Locate every Plasmodium parasite and every leukocyte.
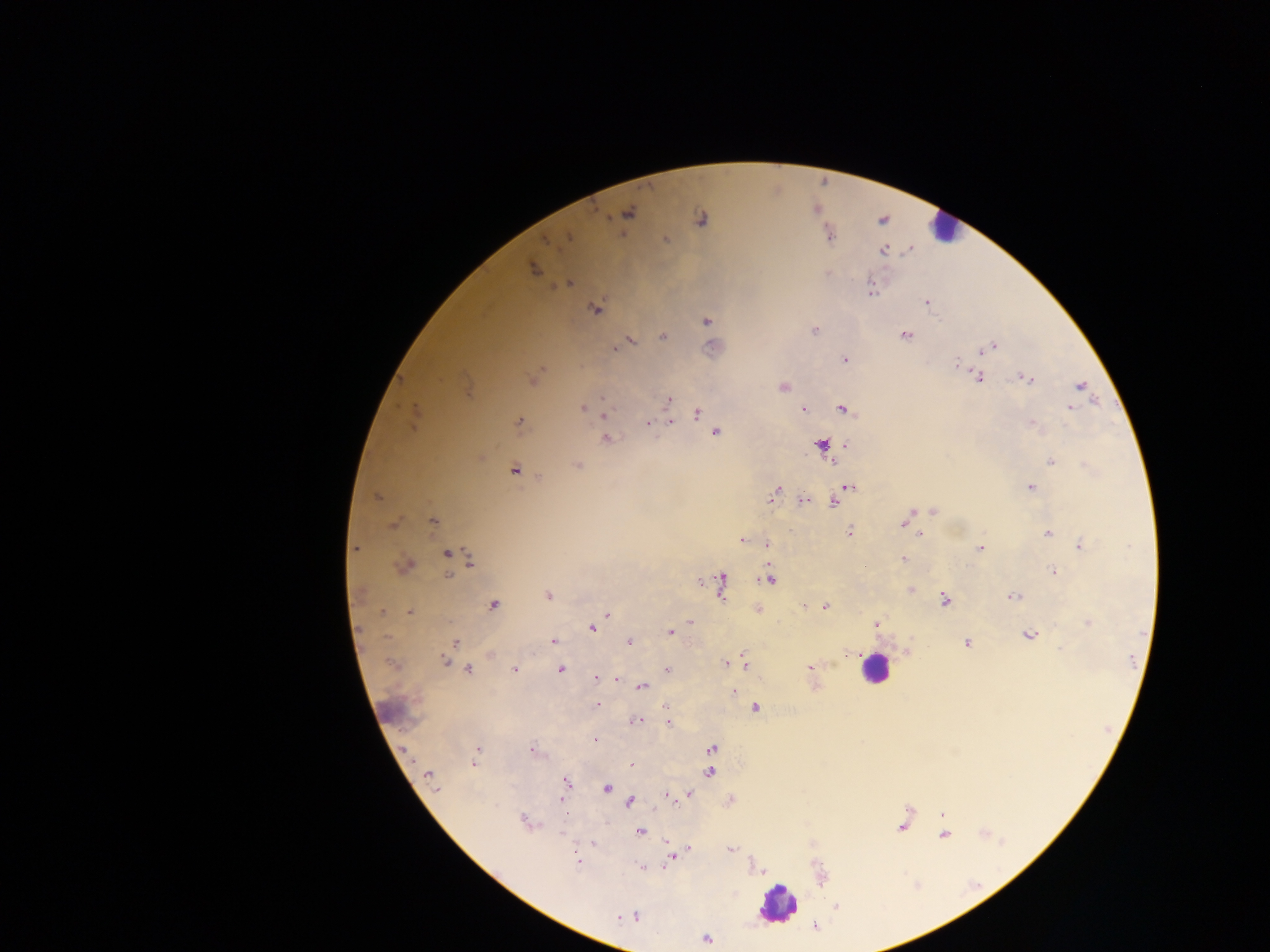

Approximate centers as (x, y) in pixels.
Plasmodium parasites: (627, 213), (701, 219), (829, 236), (568, 238), (665, 239), (884, 251), (533, 270), (569, 283), (871, 292), (927, 302), (595, 309), (707, 321), (815, 331), (905, 335), (663, 336), (631, 340), (714, 347), (993, 347), (614, 349), (984, 350), (844, 360), (956, 363), (978, 377), (1027, 379), (534, 380), (1080, 385), (783, 387), (668, 400), (603, 406), (1070, 407), (582, 408), (843, 409), (804, 411), (414, 414), (696, 414), (604, 415), (519, 421), (670, 421), (648, 423), (1032, 423), (715, 433), (606, 437), (821, 445), (847, 445), (1051, 462), (577, 465), (514, 470), (849, 486), (1031, 487), (775, 493), (843, 493), (376, 497), (804, 500), (833, 502), (933, 511), (433, 521), (393, 524), (903, 524), (909, 527), (850, 531), (1048, 533), (919, 534), (741, 540), (767, 543), (1080, 545), (355, 548), (981, 548), (446, 554), (903, 558), (470, 563), (405, 565), (1053, 571), (449, 575), (769, 579), (721, 584), (911, 590), (359, 595), (548, 595), (1014, 596), (944, 599), (494, 605), (804, 605), (825, 606), (383, 612), (409, 612), (607, 615), (690, 622), (1088, 623), (876, 624), (592, 628), (670, 632), (1029, 635), (553, 641), (455, 642), (629, 642), (967, 643), (1060, 649), (847, 653), (445, 661), (745, 662), (725, 663), (393, 665), (810, 667), (468, 669), (667, 669), (514, 670), (561, 670), (596, 677), (615, 680), (642, 687), (733, 691), (596, 705), (755, 708), (636, 721), (668, 723), (596, 740), (711, 748), (477, 749), (532, 751), (474, 763), (631, 764), (710, 772), (429, 776), (567, 782), (607, 788), (690, 794), (667, 795), (561, 800), (630, 801), (941, 814), (524, 820), (902, 826), (641, 831), (944, 835), (592, 843), (671, 849), (731, 849), (687, 850), (671, 855), (577, 862), (642, 867), (837, 906), (635, 916), (619, 918), (706, 939).
Leukocytes: (943, 229), (874, 668), (777, 904).

Summary:
  - Image size: 1270×952 pixels
  - Preparation: thick blood smear
  - Country: Ghana
  - Field of view: single
  - Capture: mobile-phone photograph through a microscope